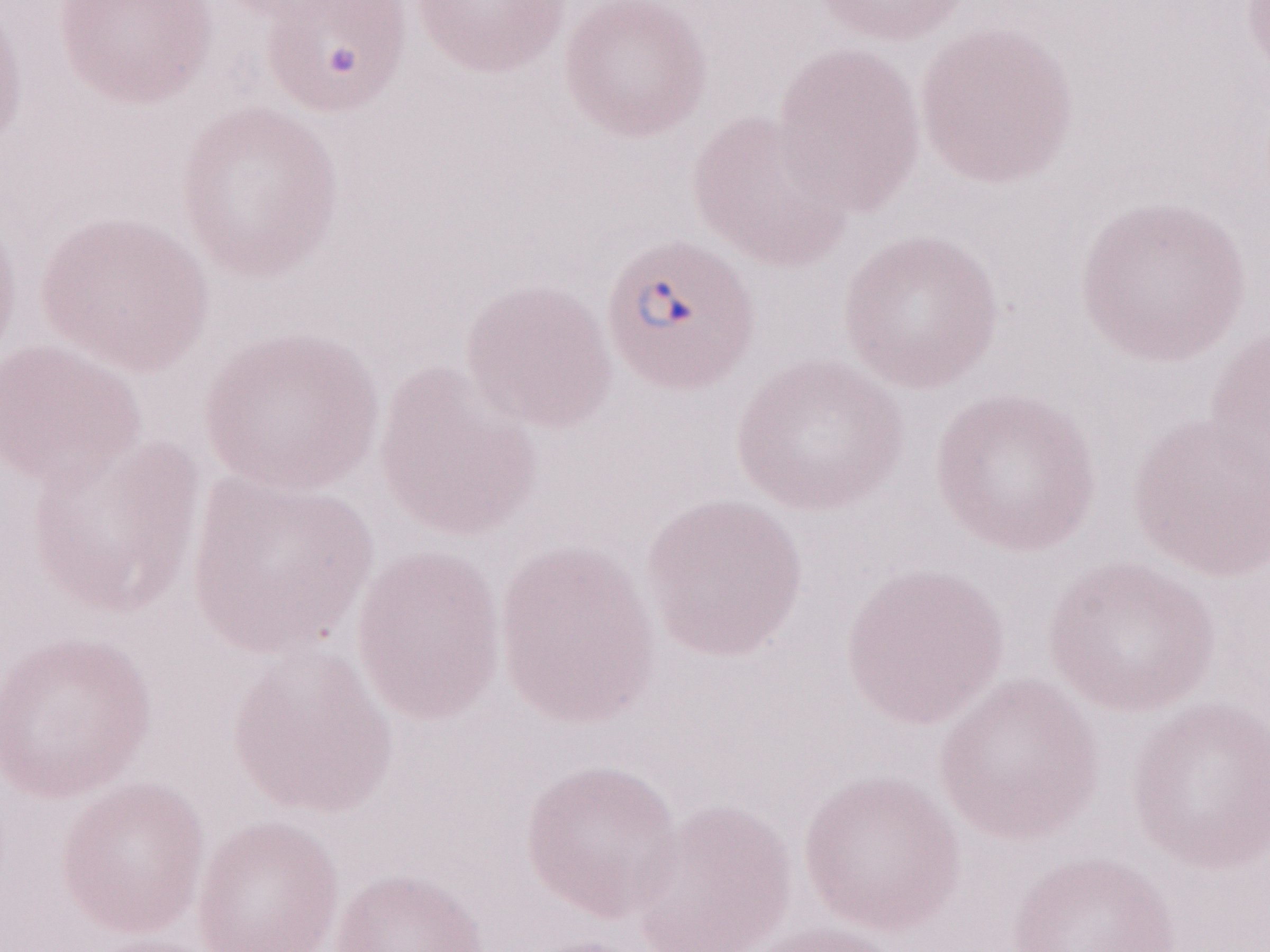
Thin blood film. Image is 1270×952 pixels. Single field of view. Patient-level malaria diagnosis: positive. 1,000x magnification. Olympus BX43 microscope and DP73 digital camera. May-Grünwald-Giemsa (MGG) stain.